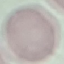
result = no malaria parasites seen
preparation = thin smear
capture = smartphone through the microscope eyepiece
stain = Giemsa
image type = automatically extracted cell patch, resized to 64 × 64 pixels